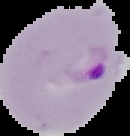

Image is 130×136 pixels. Malaria status: parasitized. The area outside the segmented cell region is set to black. From a thin blood smear.